Identify the blood parasite species.
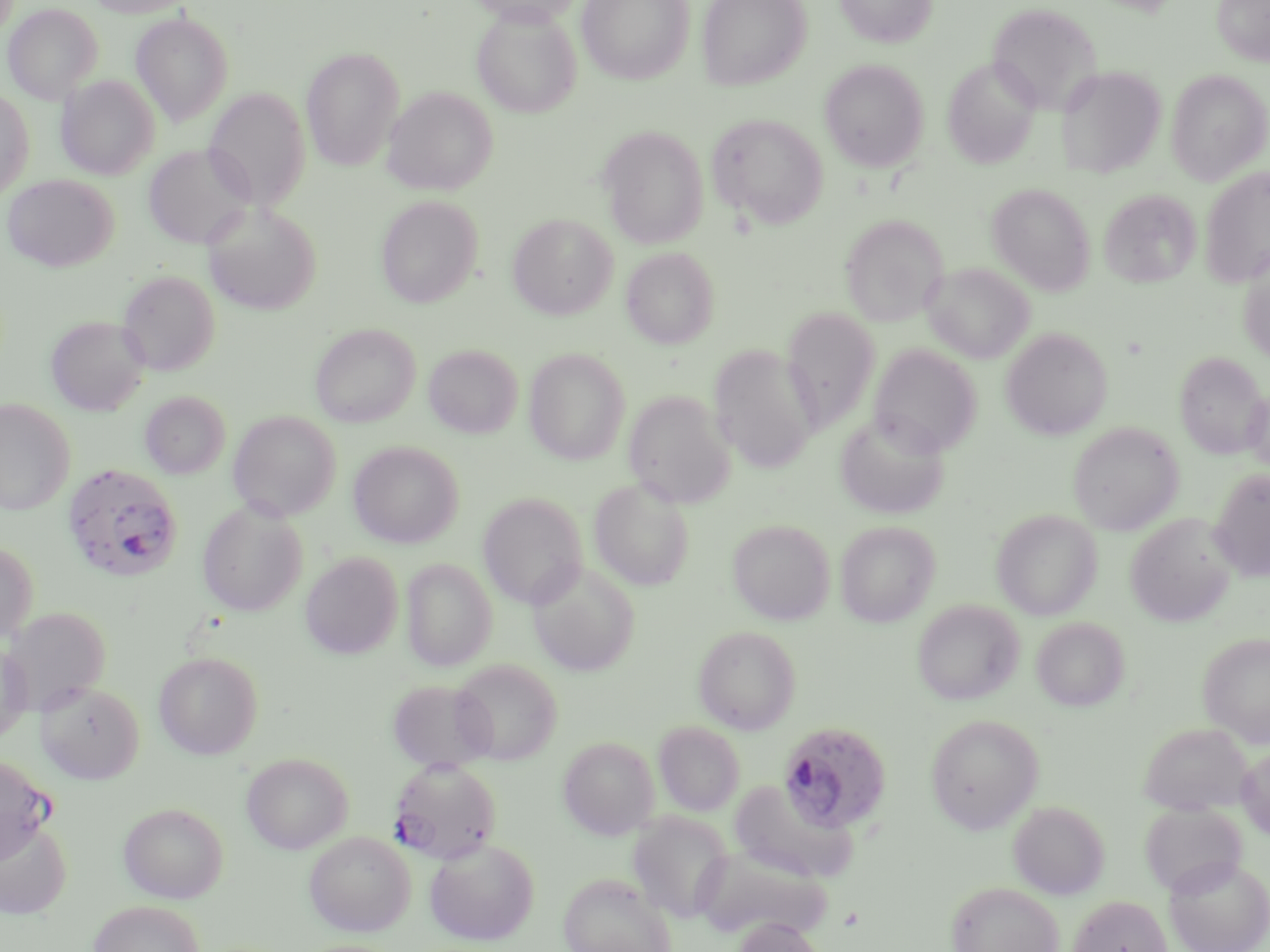
Plasmodium falciparum.

Approximate bounding boxes as named x1/y1/x2/y2 corners in pixels. Plasmodium falciparum-infected red blood cell locations: (x1=62, y1=463, x2=184, y2=582), (x1=776, y1=720, x2=892, y2=834), (x1=0, y1=754, x2=54, y2=864), (x1=389, y1=758, x2=502, y2=863). Uninfected red blood cell locations: (x1=85, y1=0, x2=196, y2=17), (x1=577, y1=0, x2=695, y2=84), (x1=697, y1=0, x2=810, y2=90), (x1=834, y1=0, x2=937, y2=48), (x1=1212, y1=0, x2=1270, y2=65), (x1=468, y1=1, x2=584, y2=27), (x1=3, y1=3, x2=103, y2=104), (x1=986, y1=3, x2=1102, y2=112), (x1=472, y1=7, x2=582, y2=118), (x1=130, y1=12, x2=234, y2=126), (x1=301, y1=47, x2=405, y2=170), (x1=942, y1=57, x2=1041, y2=169), (x1=819, y1=59, x2=929, y2=172), (x1=1055, y1=65, x2=1165, y2=178), (x1=1166, y1=69, x2=1270, y2=184), (x1=57, y1=75, x2=159, y2=180), (x1=383, y1=87, x2=498, y2=195), (x1=205, y1=89, x2=310, y2=210), (x1=0, y1=90, x2=34, y2=201), (x1=708, y1=113, x2=828, y2=229), (x1=598, y1=125, x2=708, y2=249), (x1=143, y1=143, x2=255, y2=249), (x1=1199, y1=165, x2=1270, y2=287), (x1=2, y1=174, x2=118, y2=272), (x1=987, y1=182, x2=1096, y2=296), (x1=1100, y1=189, x2=1202, y2=289), (x1=375, y1=196, x2=482, y2=308), (x1=203, y1=205, x2=322, y2=315), (x1=508, y1=213, x2=617, y2=320), (x1=841, y1=214, x2=948, y2=326), (x1=621, y1=246, x2=720, y2=349), (x1=1238, y1=255, x2=1270, y2=365), (x1=923, y1=262, x2=1034, y2=363), (x1=117, y1=270, x2=220, y2=375), (x1=781, y1=308, x2=880, y2=431), (x1=46, y1=315, x2=150, y2=416), (x1=310, y1=323, x2=420, y2=427), (x1=1002, y1=328, x2=1113, y2=440), (x1=423, y1=344, x2=523, y2=438), (x1=869, y1=344, x2=982, y2=456), (x1=709, y1=345, x2=819, y2=472), (x1=524, y1=347, x2=631, y2=465), (x1=1175, y1=352, x2=1268, y2=459), (x1=1244, y1=387, x2=1270, y2=475), (x1=623, y1=390, x2=735, y2=508), (x1=139, y1=391, x2=230, y2=478), (x1=0, y1=399, x2=76, y2=516), (x1=228, y1=410, x2=340, y2=521), (x1=835, y1=412, x2=950, y2=519), (x1=1069, y1=421, x2=1183, y2=535), (x1=348, y1=441, x2=465, y2=548), (x1=1209, y1=469, x2=1270, y2=582), (x1=589, y1=477, x2=695, y2=591), (x1=477, y1=492, x2=588, y2=608), (x1=197, y1=501, x2=307, y2=616), (x1=991, y1=508, x2=1102, y2=619), (x1=1126, y1=513, x2=1237, y2=627), (x1=728, y1=518, x2=835, y2=624), (x1=835, y1=520, x2=941, y2=627), (x1=0, y1=541, x2=38, y2=645), (x1=301, y1=551, x2=402, y2=659), (x1=401, y1=557, x2=497, y2=671), (x1=527, y1=561, x2=640, y2=676), (x1=912, y1=599, x2=1025, y2=705), (x1=2, y1=606, x2=110, y2=715), (x1=1032, y1=616, x2=1130, y2=711), (x1=693, y1=625, x2=802, y2=733), (x1=1198, y1=632, x2=1270, y2=745), (x1=0, y1=643, x2=32, y2=745), (x1=154, y1=651, x2=263, y2=759), (x1=449, y1=658, x2=562, y2=764), (x1=386, y1=678, x2=496, y2=771), (x1=35, y1=680, x2=144, y2=784), (x1=924, y1=713, x2=1044, y2=833), (x1=654, y1=721, x2=745, y2=815), (x1=1138, y1=722, x2=1252, y2=815), (x1=558, y1=736, x2=660, y2=839), (x1=1236, y1=744, x2=1270, y2=840), (x1=241, y1=752, x2=353, y2=853), (x1=728, y1=780, x2=858, y2=884), (x1=1008, y1=800, x2=1110, y2=899), (x1=118, y1=802, x2=228, y2=903), (x1=1140, y1=803, x2=1248, y2=896), (x1=627, y1=811, x2=735, y2=922), (x1=0, y1=819, x2=71, y2=919), (x1=304, y1=831, x2=415, y2=936), (x1=424, y1=837, x2=540, y2=946), (x1=697, y1=847, x2=831, y2=940), (x1=1164, y1=855, x2=1270, y2=952), (x1=558, y1=872, x2=677, y2=952), (x1=946, y1=882, x2=1064, y2=952), (x1=1068, y1=894, x2=1172, y2=952), (x1=87, y1=900, x2=204, y2=952), (x1=731, y1=918, x2=827, y2=952). Image is 1270×952 pixels. Thin blood film. May-Grünwald-Giemsa-stained preparation. Light microscopy. Captured at 1000x magnification. One field of a larger specimen.